Comment on the morphology of the red blood cells.
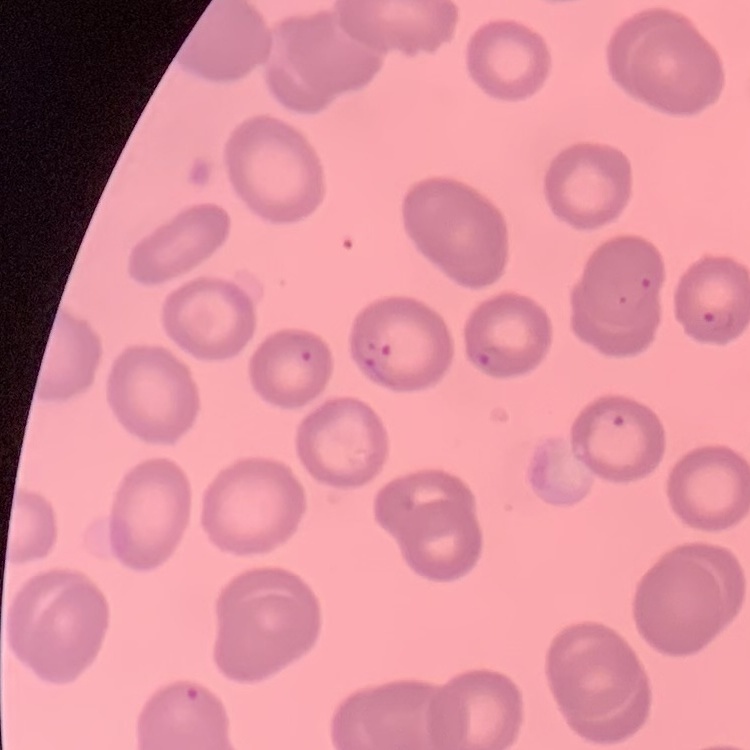

They show no rouleaux formation.

preparation = thin blood film
image type = square crop of a larger photomicrograph
stain = Field's or Giemsa